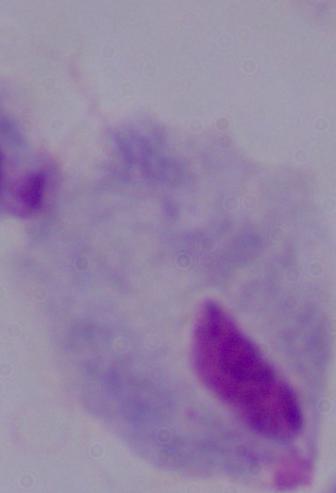
Summary:
  - Identification: trichomonad
  - Modality: micrograph
  - Magnification: 1000x